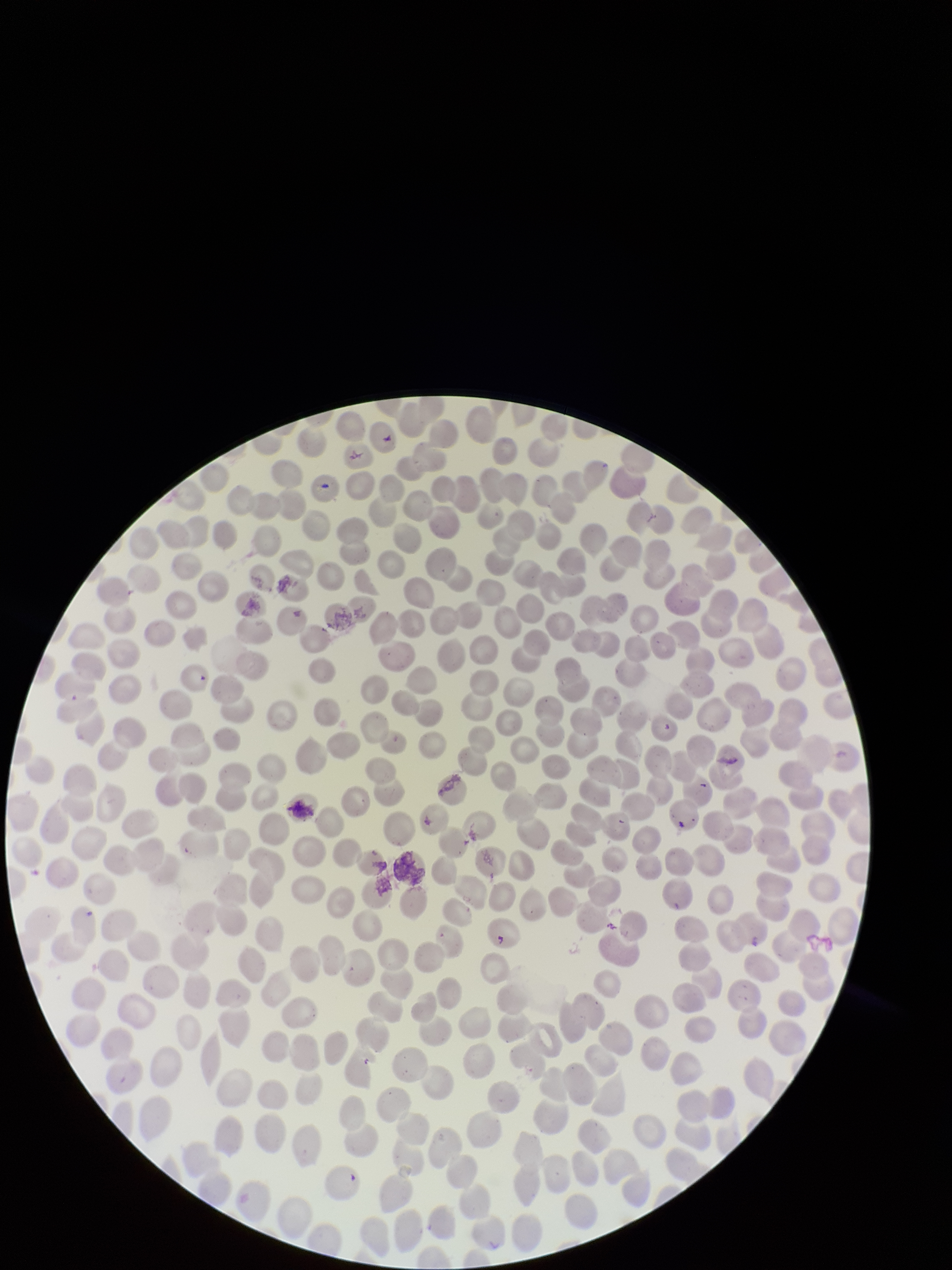
Parasitized red blood cell count: 0. Preparation: thin blood smear. Image is 952×1270 pixels. Photographed through the microscope eyepiece with a smartphone camera. Red blood cell count: 311. Patient malaria status: negative. One field from this slide. Giemsa stain. Parasitized red blood cells: none detected.